Outline each blood parasite and name the species.
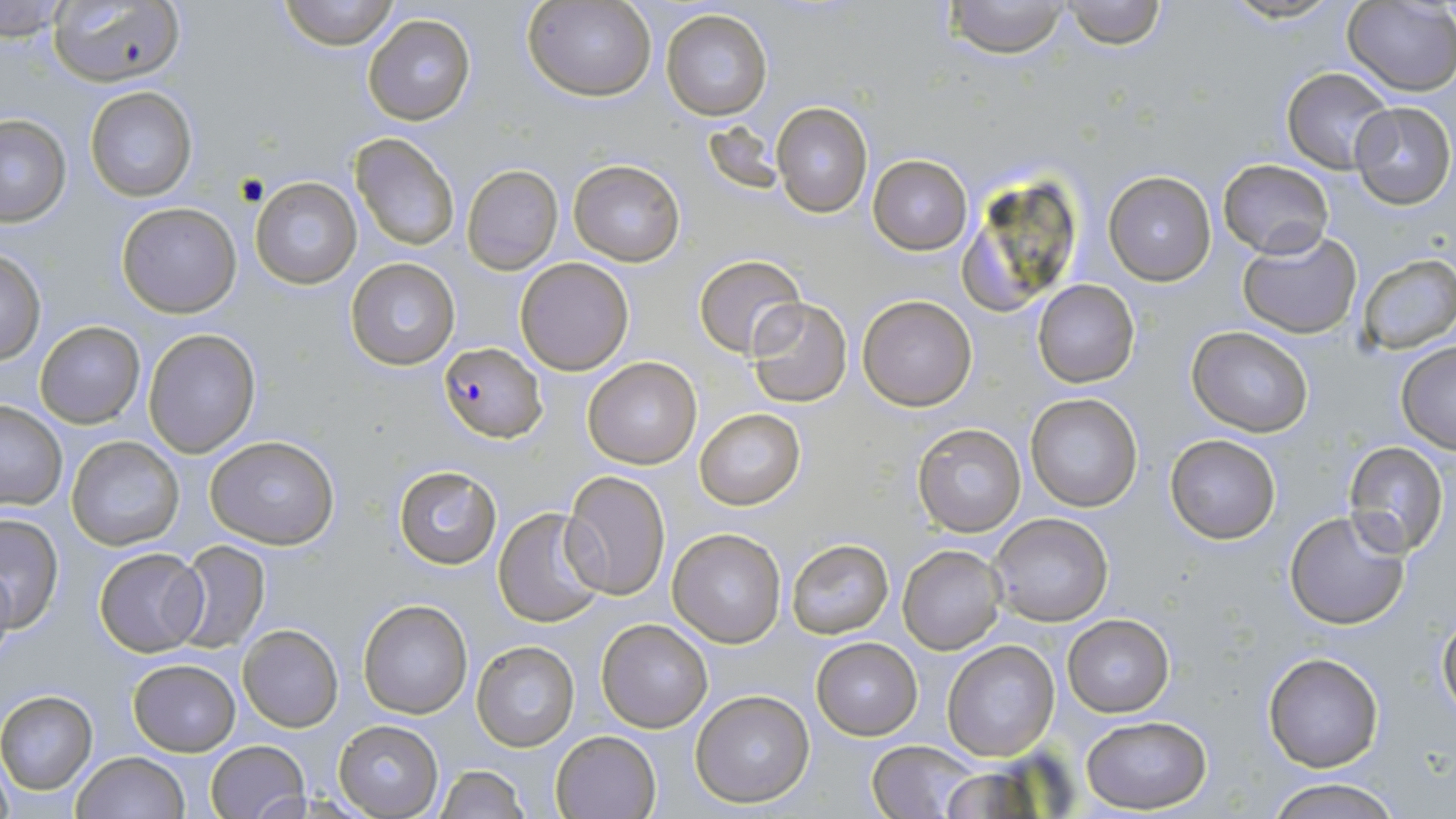

Approximate bounding boxes as (x1, y1, x2, y2) in pixels.
Plasmodium falciparum-infected red blood cells: (439, 340, 547, 455).
No Plasmodium ovale, Plasmodium malariae, Plasmodium vivax, Babesia divergens, or Trypanosoma brucei observed.

Summary:
  - Uninfected red blood cell locations: (48, 0, 188, 90), (276, 0, 402, 50), (526, 0, 655, 101), (942, 0, 1073, 58), (1061, 0, 1165, 49), (1217, 0, 1348, 25), (1343, 0, 1456, 95), (0, 1, 71, 39), (661, 9, 774, 122), (364, 14, 476, 125), (1280, 67, 1393, 172), (84, 86, 198, 202), (772, 101, 872, 218), (1349, 101, 1454, 207), (0, 115, 72, 226), (350, 132, 460, 252), (869, 154, 973, 254), (1218, 158, 1333, 258), (569, 160, 684, 266), (461, 165, 564, 276), (956, 169, 1086, 319), (1103, 172, 1217, 286), (249, 175, 362, 290), (115, 202, 241, 317), (1237, 231, 1364, 338), (0, 250, 46, 366), (1356, 253, 1456, 353), (694, 255, 807, 359), (344, 256, 461, 369), (516, 257, 635, 375), (1031, 279, 1140, 387), (857, 295, 978, 410), (746, 296, 853, 406), (36, 320, 145, 427), (1187, 326, 1313, 438), (144, 329, 261, 457), (1395, 340, 1456, 454), (584, 356, 702, 469), (1025, 392, 1145, 512), (0, 401, 69, 511), (696, 408, 807, 510), (912, 423, 1026, 536), (205, 434, 340, 550), (1164, 434, 1281, 544), (65, 436, 185, 552), (1341, 441, 1449, 559), (392, 466, 500, 568), (561, 470, 672, 600), (491, 506, 609, 628), (1283, 508, 1412, 631), (989, 511, 1114, 625), (0, 513, 64, 631), (667, 528, 786, 648), (172, 539, 271, 652), (788, 540, 894, 639), (898, 544, 1005, 656), (93, 547, 209, 658), (0, 558, 16, 668), (357, 600, 472, 719), (1436, 613, 1456, 726), (1063, 614, 1175, 717), (596, 618, 714, 733), (239, 623, 343, 732), (812, 637, 922, 740), (942, 640, 1060, 760), (471, 641, 579, 751), (1261, 651, 1383, 773), (128, 656, 241, 756), (690, 689, 817, 809), (0, 690, 98, 795), (1081, 716, 1213, 814), (334, 720, 442, 817), (550, 730, 660, 819), (205, 739, 311, 819), (868, 739, 978, 818), (71, 751, 189, 819), (434, 766, 530, 819), (1263, 778, 1402, 819)
  - Slide-level diagnosis: Plasmodium falciparum
  - Field of view: single
  - Stain: May-Grünwald-Giemsa
  - Modality: optical microscopy
  - Preparation: thin blood smear
  - Image size: 1456×819 pixels
  - Magnification: 1000x